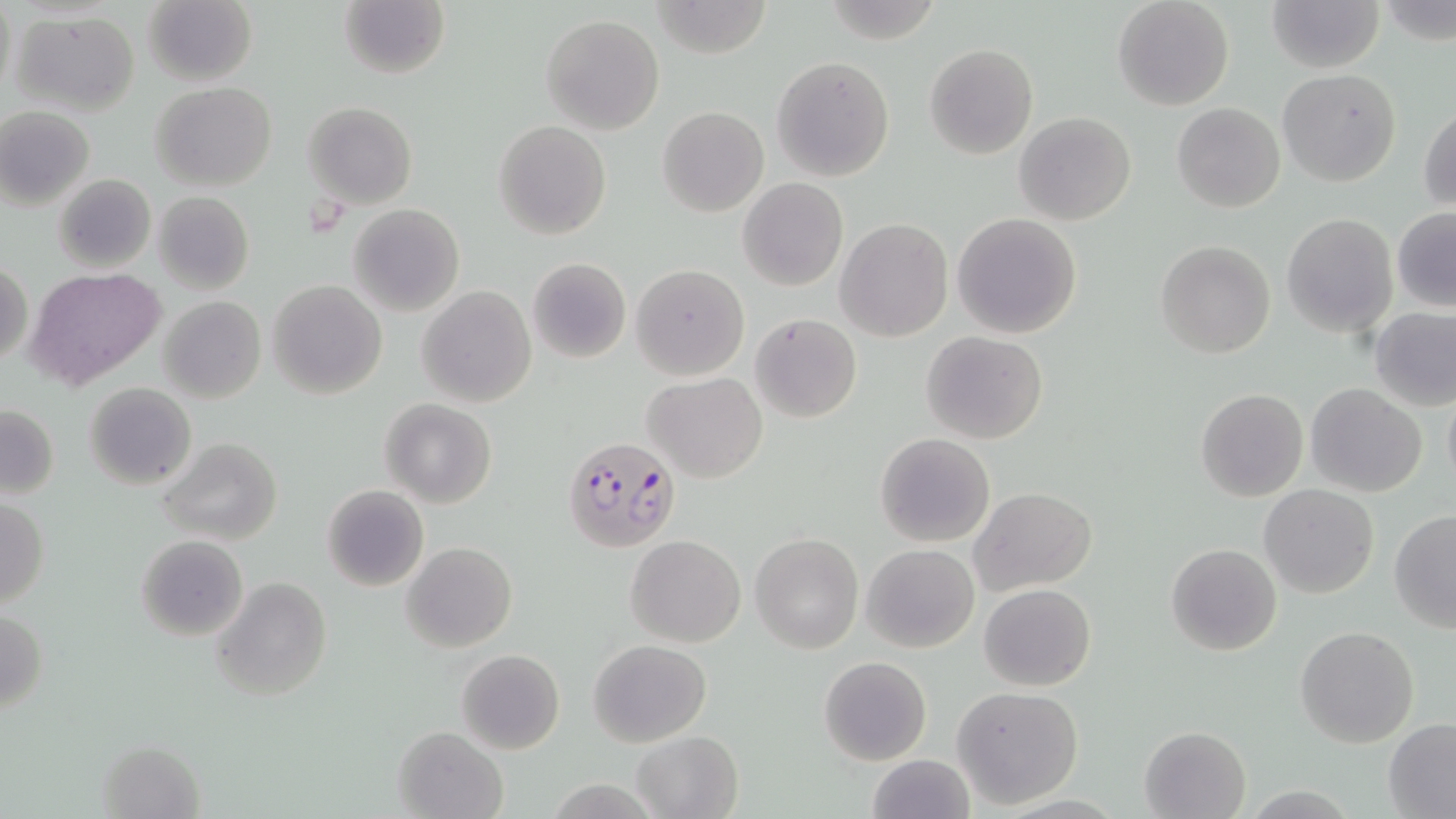

Approximate bounding boxes as (x1,y1)-(x2,y2) corner pairs in pixels. Plasmodium falciparum-infected red blood cell locations: (563,435)-(681,552). Uninfected red blood cell locations: (1,0)-(17,101), (648,0)-(771,57), (1112,0)-(1234,111), (1265,0)-(1384,73), (1380,0)-(1456,49), (142,1)-(257,87), (340,2)-(449,80), (10,9)-(142,115), (541,15)-(666,134), (924,43)-(1038,160), (770,56)-(895,182), (1278,68)-(1401,186), (149,82)-(278,192), (304,102)-(417,209), (1173,104)-(1286,213), (658,105)-(769,217), (1419,105)-(1456,213), (0,107)-(96,210), (1014,111)-(1137,226), (493,119)-(612,239), (52,174)-(156,273), (738,178)-(848,290), (153,191)-(254,294), (349,204)-(464,316), (1392,210)-(1456,310), (952,213)-(1081,338), (1282,213)-(1397,335), (835,219)-(952,342), (1155,240)-(1274,358), (526,257)-(631,364), (0,260)-(31,368), (630,264)-(750,381), (26,268)-(168,391), (269,279)-(387,399), (417,286)-(535,407), (159,295)-(266,403), (1369,307)-(1455,411), (751,313)-(862,422), (920,330)-(1049,443), (642,372)-(767,483), (84,382)-(196,491), (1306,384)-(1428,497), (1443,387)-(1456,494), (1196,388)-(1307,501), (380,399)-(497,508), (1,405)-(59,500), (875,433)-(995,547), (157,437)-(282,547), (321,485)-(430,592), (1259,485)-(1379,599), (969,487)-(1095,596), (0,497)-(50,609), (1389,510)-(1456,633), (751,533)-(864,655), (136,535)-(250,641), (625,535)-(746,647), (402,542)-(517,652), (1166,542)-(1282,656), (862,544)-(978,653), (210,575)-(332,702), (979,583)-(1096,691), (0,608)-(49,714), (1295,627)-(1419,748), (587,639)-(711,746), (456,648)-(565,755), (819,656)-(931,766), (952,685)-(1084,810), (1384,720)-(1456,816), (1140,724)-(1252,818), (392,725)-(508,819), (631,731)-(744,819), (96,739)-(205,817), (867,754)-(977,819). Slide-level diagnosis: Plasmodium falciparum. Thin blood film. One field of a larger specimen. Image is 1456×819 pixels. May-Grünwald-Giemsa stain. 1000x magnification. Optical microscopy.